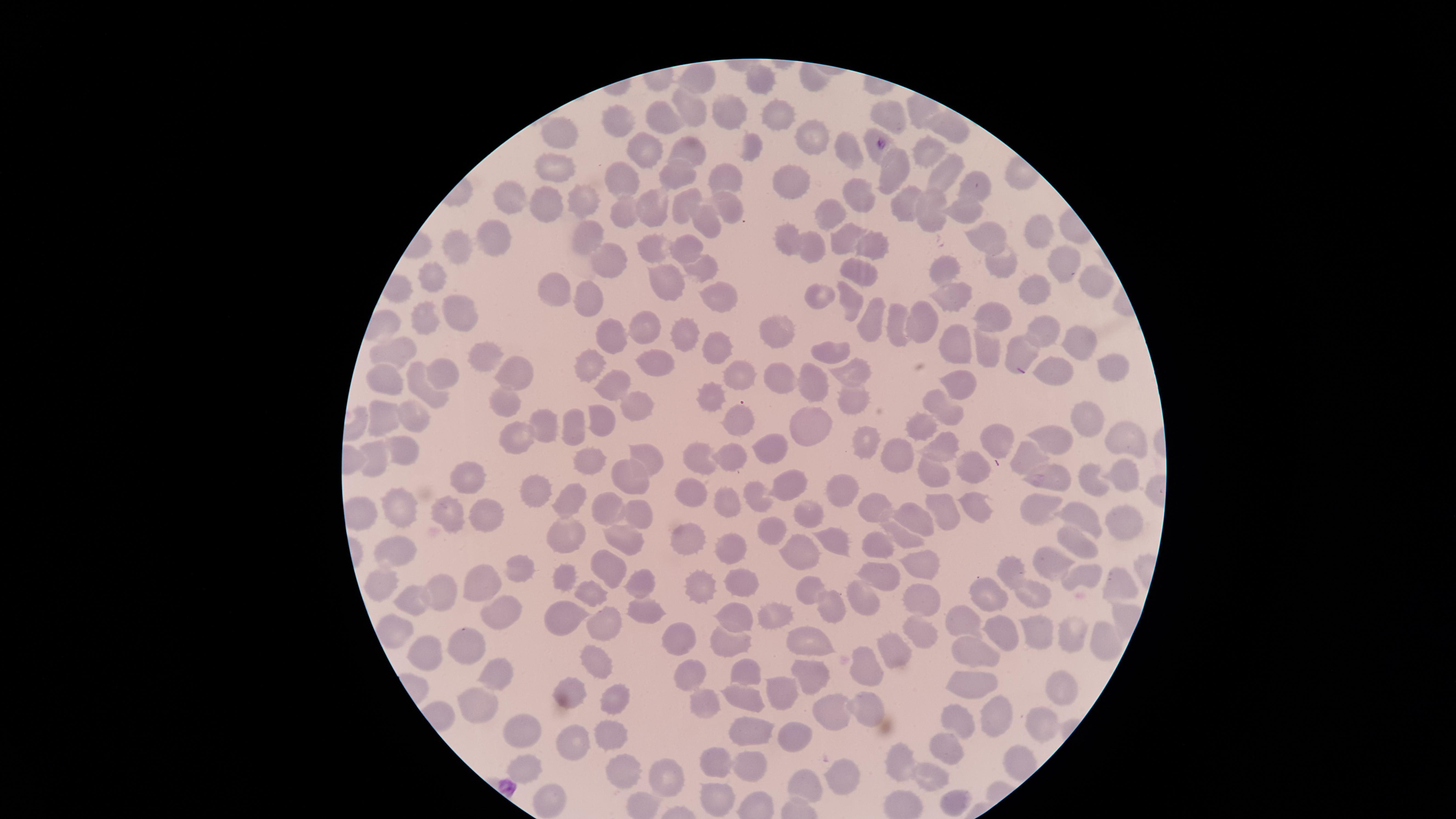

Approximate marker points, in pixels from the top-left corner. Uninfected red blood cells: (x=698, y=79), (x=765, y=80), (x=690, y=110), (x=919, y=110), (x=728, y=111), (x=886, y=113), (x=776, y=116), (x=666, y=119), (x=612, y=125), (x=947, y=128), (x=557, y=134), (x=814, y=139), (x=692, y=145), (x=846, y=149), (x=874, y=149), (x=647, y=150), (x=932, y=150), (x=754, y=152), (x=557, y=171), (x=616, y=171), (x=676, y=173), (x=894, y=173), (x=940, y=173), (x=726, y=180), (x=795, y=182), (x=983, y=182), (x=856, y=194), (x=510, y=195), (x=579, y=195), (x=686, y=199), (x=901, y=201), (x=553, y=204), (x=660, y=206), (x=623, y=207), (x=727, y=207), (x=930, y=209), (x=962, y=209), (x=828, y=212), (x=710, y=222), (x=492, y=225), (x=1044, y=231), (x=586, y=236), (x=845, y=236), (x=990, y=241), (x=459, y=243), (x=869, y=243), (x=785, y=246), (x=654, y=249), (x=683, y=249), (x=808, y=249), (x=1001, y=262), (x=612, y=263), (x=1065, y=264), (x=701, y=266), (x=945, y=267), (x=859, y=270), (x=432, y=276), (x=667, y=282), (x=1093, y=283), (x=1035, y=289), (x=556, y=290), (x=715, y=291), (x=593, y=298), (x=823, y=298), (x=847, y=298), (x=948, y=298), (x=463, y=313), (x=430, y=317), (x=874, y=317), (x=995, y=317), (x=920, y=323), (x=898, y=325), (x=776, y=326), (x=652, y=327), (x=1042, y=328), (x=688, y=334), (x=612, y=336), (x=1080, y=340), (x=955, y=343), (x=714, y=346), (x=983, y=348), (x=1027, y=349), (x=396, y=351), (x=834, y=352), (x=491, y=357), (x=654, y=357), (x=593, y=363), (x=1105, y=365), (x=1052, y=369), (x=852, y=371), (x=736, y=373), (x=441, y=374), (x=516, y=376), (x=391, y=377), (x=776, y=379), (x=963, y=385), (x=606, y=386), (x=820, y=386), (x=431, y=393), (x=853, y=402), (x=503, y=403), (x=715, y=404), (x=639, y=408), (x=408, y=409), (x=946, y=409), (x=385, y=416), (x=603, y=418), (x=1089, y=418), (x=578, y=420), (x=738, y=424), (x=921, y=425), (x=542, y=427), (x=804, y=430), (x=509, y=436), (x=995, y=437), (x=1128, y=438), (x=1059, y=440), (x=865, y=441), (x=774, y=444), (x=937, y=444), (x=404, y=447), (x=735, y=449), (x=902, y=449), (x=586, y=452), (x=700, y=453), (x=377, y=454), (x=645, y=454), (x=1036, y=456), (x=973, y=463), (x=634, y=472), (x=1056, y=472), (x=930, y=473), (x=1123, y=474), (x=465, y=475), (x=1091, y=478), (x=793, y=482), (x=841, y=485), (x=695, y=492), (x=536, y=494), (x=754, y=496), (x=571, y=499), (x=726, y=501), (x=973, y=503), (x=611, y=504), (x=403, y=505), (x=877, y=505), (x=1045, y=507), (x=944, y=508), (x=639, y=509), (x=483, y=511), (x=806, y=512), (x=364, y=515), (x=446, y=515), (x=1078, y=517), (x=916, y=518), (x=1120, y=523), (x=774, y=530), (x=561, y=533), (x=621, y=535), (x=900, y=536), (x=830, y=538), (x=688, y=542), (x=727, y=544), (x=1078, y=545), (x=879, y=547), (x=401, y=549), (x=802, y=553), (x=607, y=565), (x=916, y=565), (x=1054, y=565), (x=529, y=568), (x=1010, y=569), (x=1083, y=575), (x=567, y=578), (x=880, y=578), (x=643, y=580), (x=741, y=582), (x=481, y=583), (x=385, y=584), (x=1120, y=585), (x=806, y=589), (x=592, y=590), (x=703, y=590), (x=1032, y=590), (x=440, y=591), (x=988, y=592), (x=419, y=600), (x=919, y=602), (x=864, y=605), (x=636, y=607), (x=503, y=609), (x=825, y=609), (x=776, y=612), (x=563, y=614), (x=605, y=617), (x=733, y=620), (x=971, y=624), (x=394, y=631), (x=1039, y=631), (x=918, y=635), (x=1078, y=635), (x=1006, y=637), (x=1101, y=637), (x=683, y=639), (x=470, y=643), (x=812, y=644), (x=423, y=649), (x=726, y=649), (x=971, y=649), (x=889, y=652), (x=596, y=661), (x=864, y=662), (x=741, y=671), (x=490, y=672), (x=697, y=677), (x=807, y=677), (x=972, y=680), (x=1060, y=684), (x=739, y=691), (x=782, y=696), (x=577, y=697), (x=612, y=697), (x=483, y=699), (x=702, y=700), (x=828, y=709), (x=864, y=710), (x=989, y=713), (x=960, y=719), (x=1039, y=721), (x=523, y=732), (x=604, y=732), (x=753, y=732), (x=794, y=737), (x=576, y=743), (x=942, y=751), (x=902, y=759), (x=753, y=760), (x=725, y=764), (x=1019, y=764), (x=524, y=768), (x=622, y=770), (x=925, y=773), (x=669, y=774), (x=838, y=774), (x=805, y=783), (x=718, y=798), (x=954, y=798), (x=556, y=800), (x=647, y=801). Giemsa-stained preparation. Smartphone photograph through the microscope eyepiece. Image is 1456×819 pixels. Presence: no malaria parasites identified. One field of view of the specimen. Thin blood film. The visible region is circular.